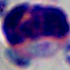

identification: white blood cell
magnification: 1000x
modality: photomicrograph